Assess this cell for malaria.
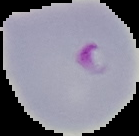

It is parasitized.

Summary:
  - Preparation: thin blood film
  - Image type: cell region segmented out of the field of view; surrounding area masked to black
  - Image size: 139×136 pixels